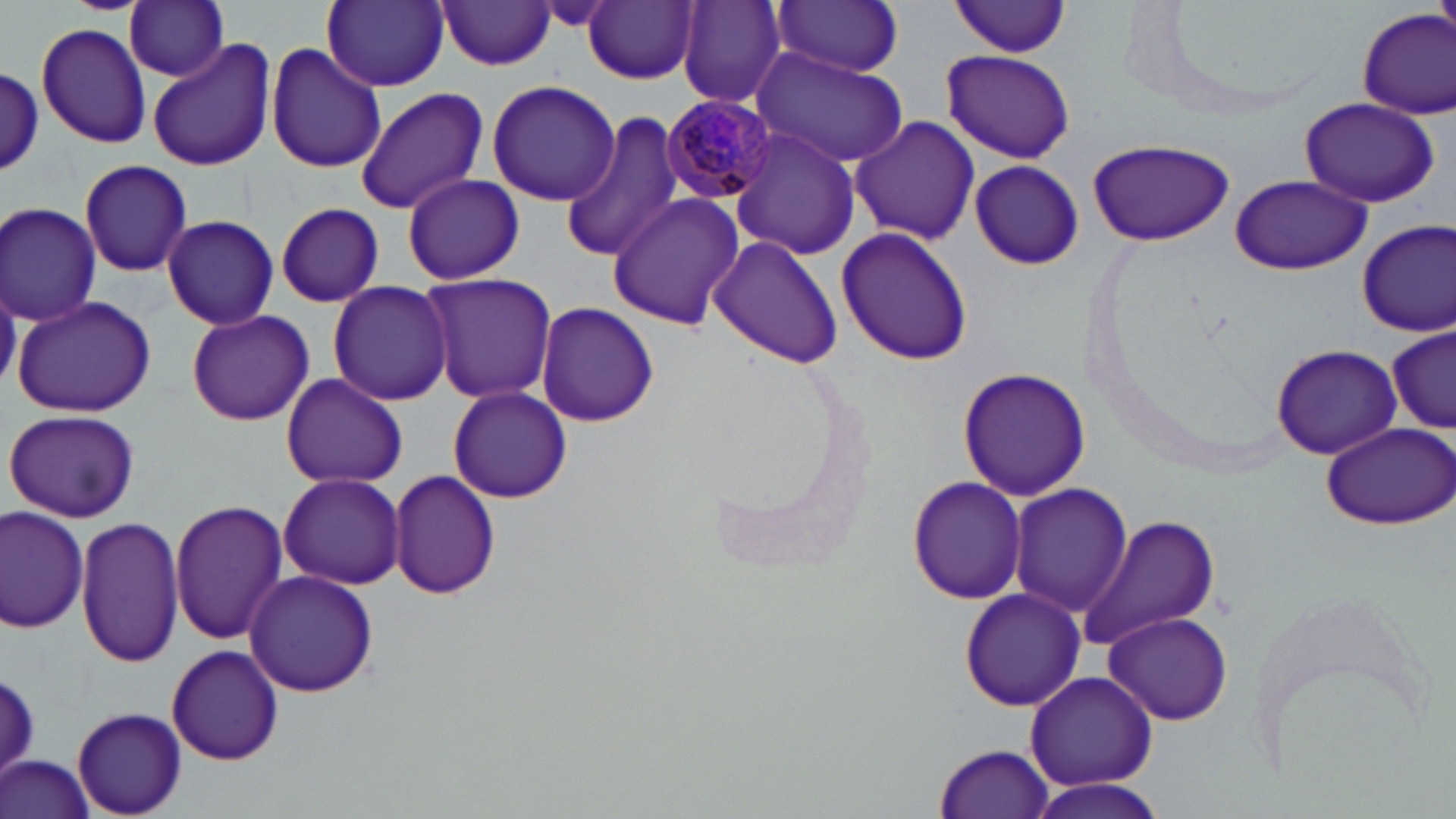

Summary:
  - Coordinate format: approximate bounding boxes as (x1, y1, x2, y2) in pixels
  - Plasmodium malariae-infected red blood cell locations: (662, 94, 776, 204)
  - Uninfected red blood cell locations: (323, 0, 448, 90), (677, 0, 788, 110), (124, 1, 229, 81), (772, 1, 905, 76), (949, 1, 1073, 58), (437, 2, 556, 70), (585, 2, 698, 85), (1354, 7, 1456, 119), (37, 23, 151, 149), (148, 41, 276, 172), (264, 41, 386, 175), (750, 46, 912, 170), (940, 49, 1076, 164), (1, 68, 47, 176), (487, 81, 621, 206), (354, 87, 487, 214), (1300, 99, 1438, 208), (560, 113, 691, 263), (851, 117, 981, 247), (729, 127, 861, 261), (1086, 137, 1236, 248), (78, 158, 192, 279), (969, 159, 1083, 271), (402, 173, 524, 285), (1230, 174, 1370, 275), (608, 194, 744, 331), (1, 201, 102, 326), (276, 202, 383, 307), (161, 215, 280, 331), (1357, 220, 1455, 338), (835, 226, 974, 366), (707, 234, 844, 369), (419, 271, 557, 403), (327, 280, 454, 406), (11, 295, 155, 419), (536, 302, 659, 427), (186, 308, 314, 426), (1387, 327, 1456, 432), (1271, 342, 1401, 460), (957, 367, 1093, 503), (281, 374, 408, 489), (446, 386, 574, 502), (5, 408, 141, 524), (1319, 421, 1454, 530), (387, 468, 502, 600), (277, 471, 404, 588), (907, 474, 1029, 606), (1007, 482, 1132, 617), (169, 497, 290, 644), (0, 506, 89, 632), (1079, 514, 1220, 651), (77, 518, 185, 668), (244, 570, 377, 698), (958, 589, 1086, 713), (1100, 611, 1235, 727), (165, 643, 285, 765), (1, 669, 40, 779), (1025, 670, 1157, 790), (72, 708, 187, 816), (934, 743, 1056, 818), (2, 757, 97, 819), (1021, 777, 1176, 819)
  - Slide-level diagnosis: Plasmodium malariae
  - Magnification: 1000x
  - Field of view: single
  - Image size: 1456×819 pixels
  - Preparation: thin blood film
  - Stain: May-Grünwald-Giemsa
  - Modality: optical microscopy